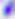
{
  "magnification": "400x",
  "modality": "micrograph",
  "identification": "Toxoplasma gondii"
}